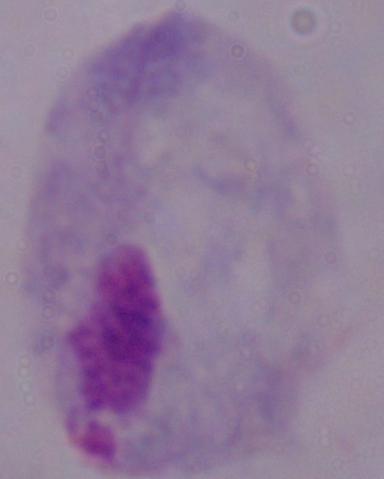
Captured at 1000x magnification. A trichomonad is shown. Photomicrograph.